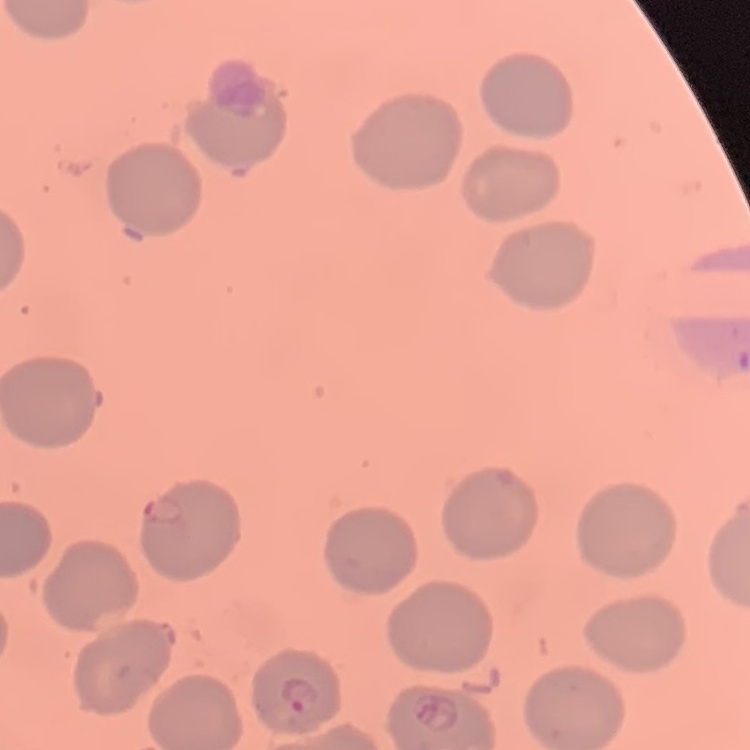
The erythrocytes exhibit no rouleaux formation. Stained with either Field's or Giemsa. One tile cut from a larger photomicrograph. Thin blood film.